Assess this cell for malaria.
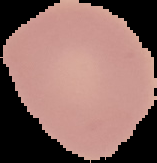

It is uninfected.

From a thin blood smear. Image is 157×163 pixels. Cell region segmented out of the field of view; the surrounding area is masked to black.